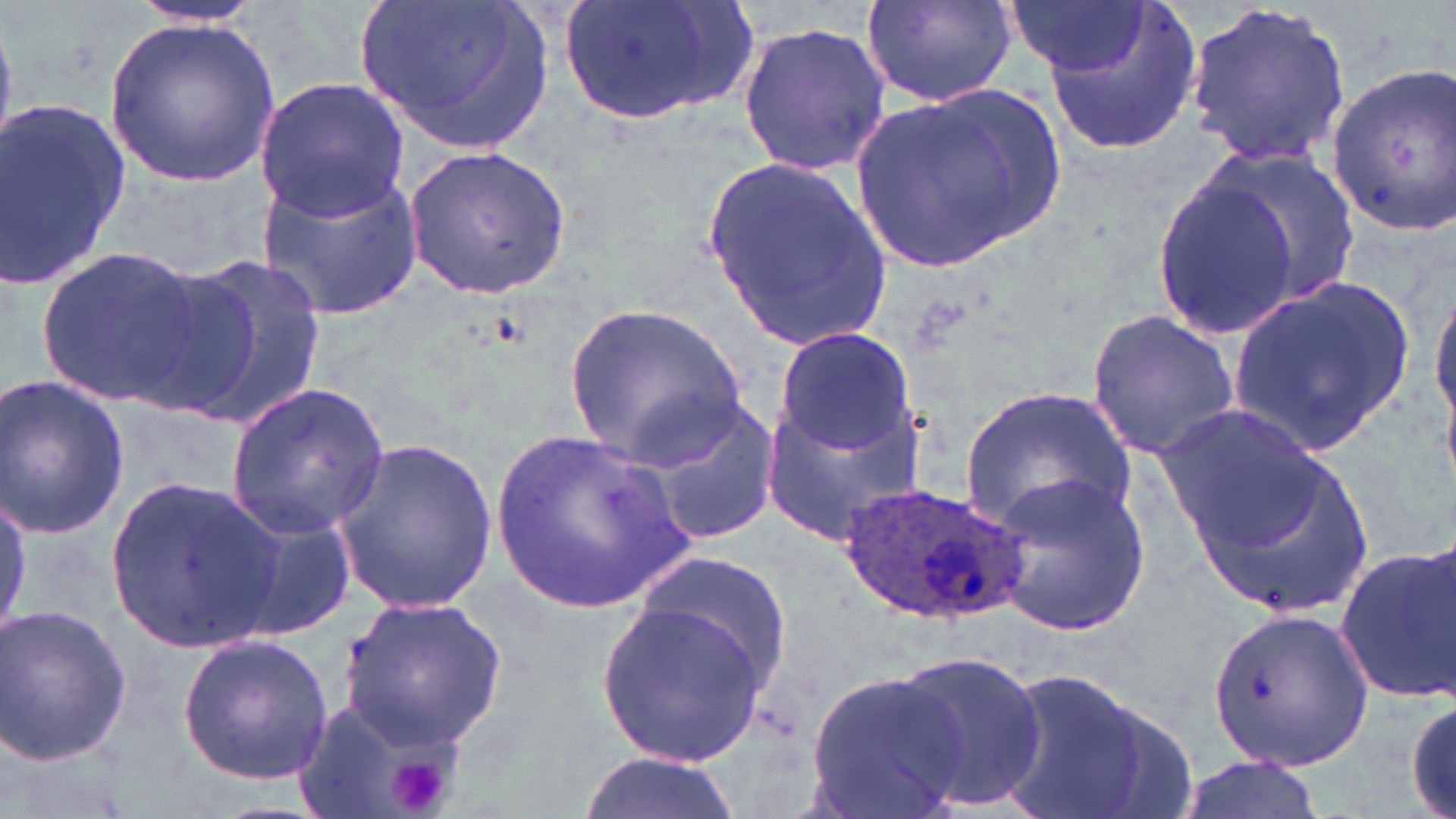
slide_level_diagnosis: Plasmodium ovale
field_of_view: single
preparation: thin blood smear
magnification: 1000x
modality: light microscopy
plasmodium_ovale_infected_red_blood_cell_locations: 'approximate bounding boxes as named x1/y1/x2/y2 corners in pixels: (x1=839, y1=479, x2=1033, y2=627)'
uninfected_red_blood_cell_locations: 'approximate bounding boxes as named x1/y1/x2/y2 corners in pixels: (x1=357, y1=0, x2=554, y2=157), (x1=560, y1=0, x2=757, y2=130), (x1=858, y1=0, x2=1022, y2=109), (x1=1006, y1=0, x2=1152, y2=75), (x1=125, y1=1, x2=268, y2=31), (x1=1037, y1=1, x2=1203, y2=160), (x1=1183, y1=1, x2=1353, y2=170), (x1=105, y1=15, x2=279, y2=187), (x1=735, y1=19, x2=889, y2=177), (x1=1325, y1=62, x2=1456, y2=234), (x1=255, y1=77, x2=411, y2=219), (x1=848, y1=81, x2=1065, y2=278), (x1=0, y1=97, x2=133, y2=294), (x1=403, y1=141, x2=575, y2=300), (x1=1182, y1=143, x2=1364, y2=318), (x1=700, y1=153, x2=892, y2=354), (x1=254, y1=162, x2=425, y2=321), (x1=1150, y1=173, x2=1304, y2=340), (x1=36, y1=249, x2=208, y2=407), (x1=158, y1=253, x2=331, y2=430), (x1=1431, y1=267, x2=1456, y2=449), (x1=1229, y1=274, x2=1414, y2=452), (x1=564, y1=303, x2=747, y2=463), (x1=1086, y1=307, x2=1243, y2=462), (x1=773, y1=327, x2=917, y2=459), (x1=0, y1=375, x2=131, y2=536), (x1=225, y1=384, x2=390, y2=538), (x1=959, y1=384, x2=1136, y2=532), (x1=623, y1=391, x2=782, y2=547), (x1=762, y1=395, x2=928, y2=547), (x1=1154, y1=401, x2=1333, y2=560), (x1=491, y1=426, x2=700, y2=612), (x1=329, y1=436, x2=498, y2=614), (x1=1182, y1=440, x2=1379, y2=624), (x1=983, y1=466, x2=1150, y2=636), (x1=106, y1=474, x2=283, y2=655), (x1=227, y1=499, x2=360, y2=641), (x1=1334, y1=543, x2=1455, y2=706), (x1=632, y1=546, x2=796, y2=698), (x1=338, y1=594, x2=509, y2=748), (x1=595, y1=597, x2=773, y2=771), (x1=1, y1=603, x2=133, y2=767), (x1=1205, y1=603, x2=1370, y2=773), (x1=176, y1=633, x2=334, y2=788), (x1=889, y1=650, x2=1048, y2=811), (x1=990, y1=663, x2=1168, y2=819), (x1=806, y1=667, x2=965, y2=815), (x1=1406, y1=691, x2=1455, y2=819), (x1=293, y1=692, x2=470, y2=819), (x1=579, y1=752, x2=743, y2=819), (x1=1172, y1=753, x2=1323, y2=819)'
stain: May-Grünwald-Giemsa
platelet_locations: 'approximate bounding boxes as named x1/y1/x2/y2 corners in pixels: (x1=384, y1=750, x2=455, y2=818)'
image_size: 1456×819 pixels